Give the position of every Plasmodium parasite visible.
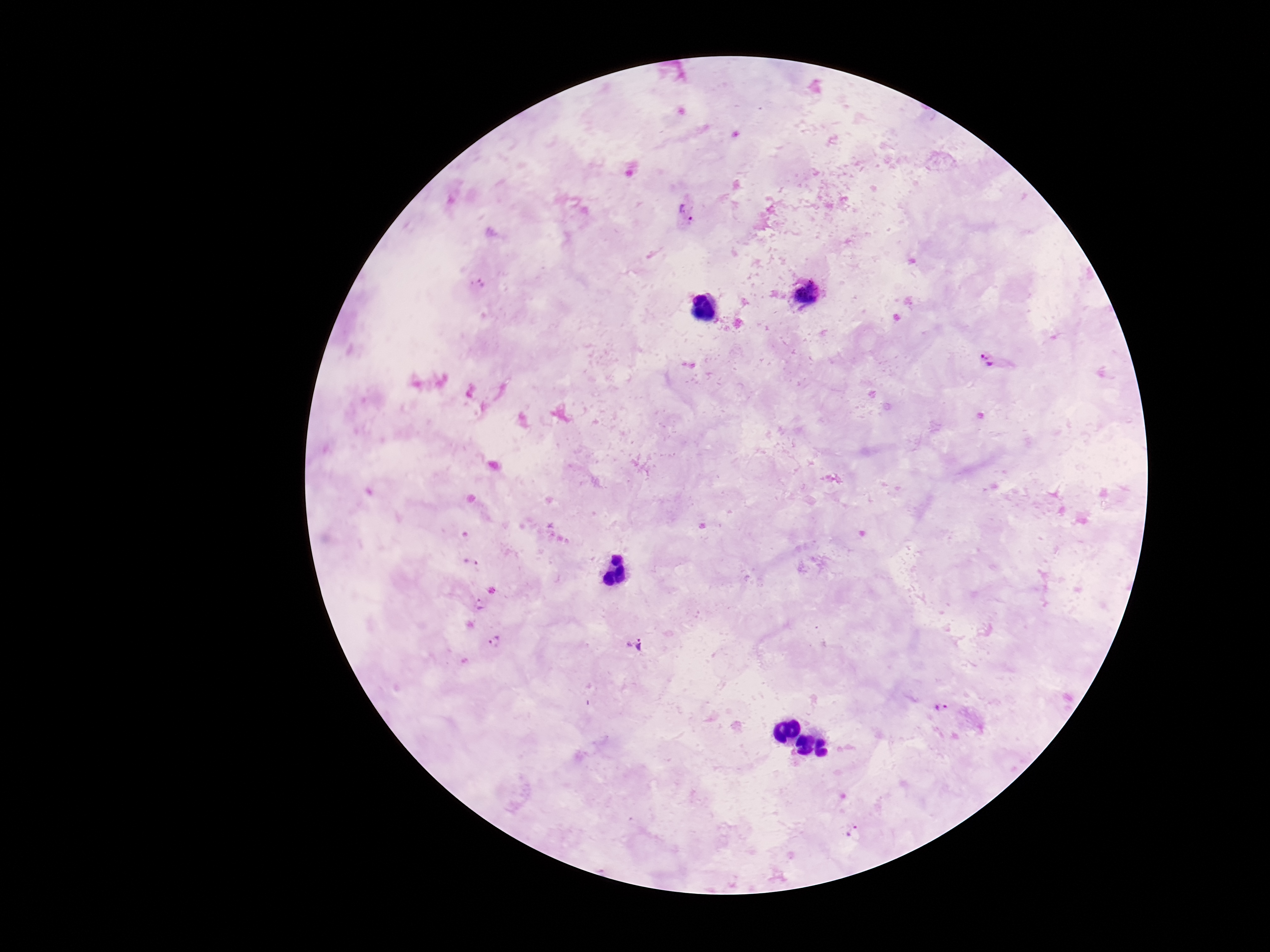
Approximate object centers, in pixels from the top-left corner.
Plasmodium parasites: (x=685, y=212), (x=478, y=283), (x=805, y=294), (x=993, y=361), (x=471, y=562), (x=479, y=605), (x=495, y=641), (x=634, y=643), (x=940, y=707), (x=853, y=831).

Thick peripheral-blood smear. Giemsa stain. Single field of view. Patient malaria status: infected. Image is 1270×952 pixels. Photographed through the microscope eyepiece with a smartphone camera. 100x magnification.